Assess the morphology of the erythrocytes.
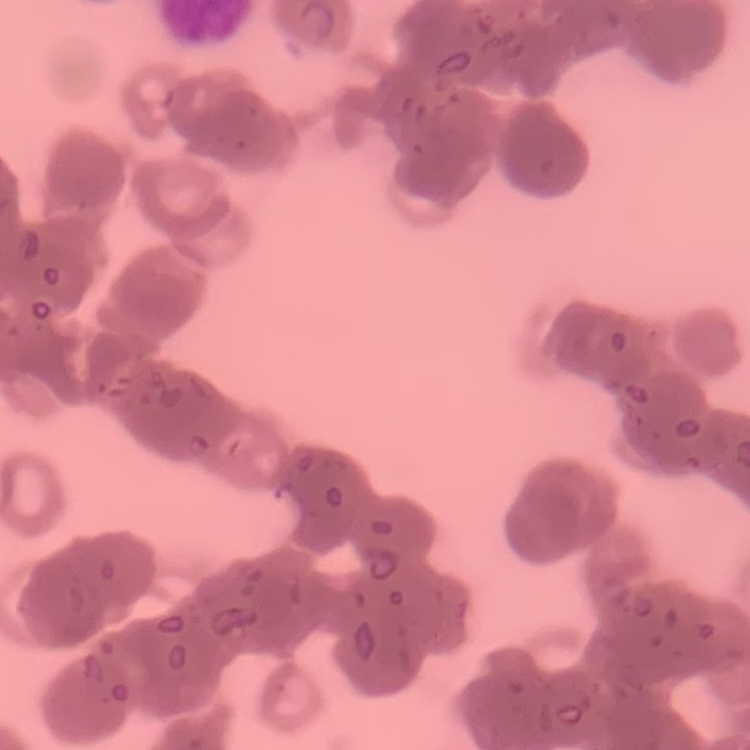

They show rouleaux formation.

Summary:
  - Stain: Field's or Giemsa
  - Image type: square crop of a larger photomicrograph
  - Preparation: thin blood film